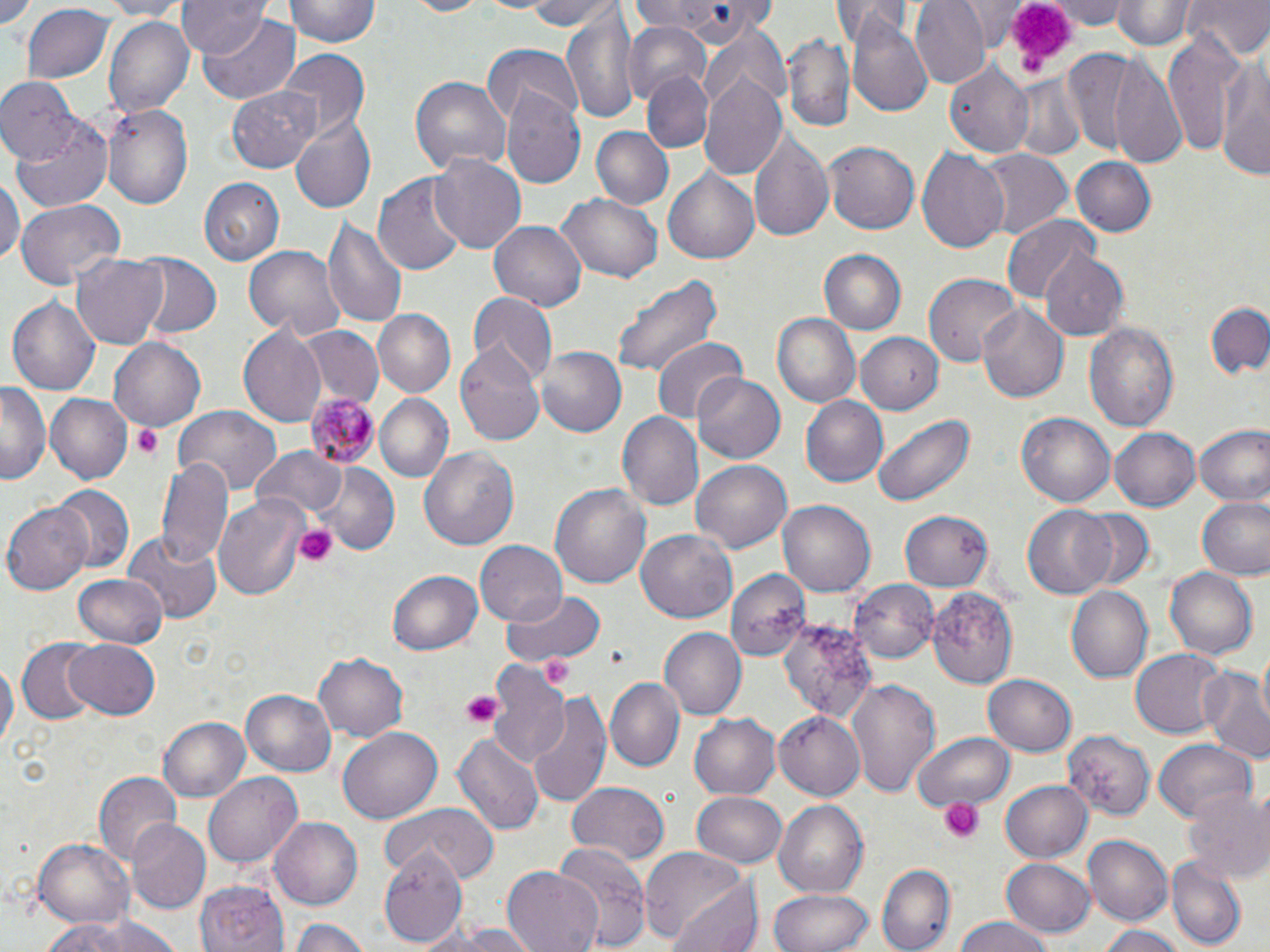

slide-level diagnosis = Plasmodium malariae
platelet locations = approximate bounding boxes as named x1/y1/x2/y2 corners in pixels: (x1=999, y1=4, x2=1075, y2=81), (x1=132, y1=425, x2=162, y2=460), (x1=294, y1=524, x2=337, y2=567), (x1=542, y1=654, x2=574, y2=688), (x1=461, y1=691, x2=500, y2=727), (x1=940, y1=797, x2=982, y2=844)
stain = May-Grünwald-Giemsa
image size = 1270×952 pixels
preparation = thin blood film
modality = light microscopy
field of view = single
Plasmodium malariae-infected red blood cell locations = approximate bounding boxes as named x1/y1/x2/y2 corners in pixels: (x1=306, y1=394, x2=379, y2=467)
magnification = 1000x
uninfected red blood cell locations = approximate bounding boxes as named x1/y1/x2/y2 corners in pixels: (x1=2, y1=0, x2=45, y2=39), (x1=91, y1=0, x2=187, y2=18), (x1=179, y1=0, x2=268, y2=58), (x1=284, y1=0, x2=382, y2=48), (x1=398, y1=0, x2=499, y2=18), (x1=518, y1=0, x2=620, y2=28), (x1=910, y1=0, x2=989, y2=87), (x1=1049, y1=0, x2=1130, y2=29), (x1=1112, y1=0, x2=1194, y2=50), (x1=1183, y1=0, x2=1269, y2=60), (x1=628, y1=1, x2=778, y2=41), (x1=833, y1=1, x2=917, y2=46), (x1=21, y1=4, x2=116, y2=86), (x1=561, y1=11, x2=642, y2=125), (x1=196, y1=13, x2=300, y2=103), (x1=103, y1=14, x2=194, y2=117), (x1=848, y1=17, x2=935, y2=116), (x1=623, y1=22, x2=714, y2=99), (x1=1164, y1=28, x2=1244, y2=162), (x1=780, y1=32, x2=854, y2=133), (x1=696, y1=44, x2=789, y2=181), (x1=482, y1=46, x2=583, y2=127), (x1=1218, y1=48, x2=1270, y2=182), (x1=278, y1=49, x2=369, y2=138), (x1=1077, y1=53, x2=1186, y2=164), (x1=946, y1=61, x2=1034, y2=157), (x1=642, y1=72, x2=713, y2=153), (x1=1007, y1=74, x2=1088, y2=162), (x1=411, y1=76, x2=511, y2=174), (x1=0, y1=79, x2=80, y2=167), (x1=227, y1=85, x2=323, y2=172), (x1=501, y1=89, x2=586, y2=189), (x1=101, y1=103, x2=193, y2=207), (x1=12, y1=114, x2=114, y2=210), (x1=292, y1=117, x2=377, y2=213), (x1=588, y1=126, x2=674, y2=211), (x1=747, y1=129, x2=833, y2=245), (x1=824, y1=140, x2=919, y2=235), (x1=916, y1=147, x2=1010, y2=256), (x1=977, y1=149, x2=1071, y2=237), (x1=431, y1=154, x2=527, y2=253), (x1=1071, y1=156, x2=1158, y2=238), (x1=662, y1=167, x2=761, y2=264), (x1=375, y1=172, x2=468, y2=275), (x1=0, y1=177, x2=22, y2=267), (x1=199, y1=178, x2=284, y2=266), (x1=556, y1=189, x2=662, y2=281), (x1=14, y1=199, x2=125, y2=290), (x1=1001, y1=217, x2=1100, y2=307), (x1=323, y1=218, x2=408, y2=327), (x1=489, y1=221, x2=588, y2=310), (x1=243, y1=246, x2=345, y2=341), (x1=818, y1=249, x2=907, y2=337), (x1=1038, y1=251, x2=1129, y2=339), (x1=70, y1=252, x2=169, y2=348), (x1=127, y1=252, x2=223, y2=341), (x1=611, y1=272, x2=721, y2=379), (x1=925, y1=272, x2=1024, y2=366), (x1=469, y1=292, x2=556, y2=384), (x1=7, y1=293, x2=100, y2=400), (x1=1209, y1=303, x2=1270, y2=379), (x1=977, y1=304, x2=1069, y2=404), (x1=374, y1=309, x2=456, y2=397), (x1=771, y1=311, x2=861, y2=411), (x1=1085, y1=320, x2=1178, y2=435), (x1=300, y1=325, x2=382, y2=405), (x1=237, y1=327, x2=326, y2=429), (x1=855, y1=331, x2=943, y2=416), (x1=109, y1=336, x2=207, y2=432), (x1=650, y1=336, x2=748, y2=425), (x1=457, y1=341, x2=545, y2=445), (x1=535, y1=346, x2=626, y2=437), (x1=691, y1=372, x2=786, y2=463), (x1=1, y1=383, x2=51, y2=486), (x1=43, y1=392, x2=132, y2=484), (x1=374, y1=394, x2=453, y2=483), (x1=802, y1=395, x2=888, y2=488), (x1=173, y1=408, x2=282, y2=499), (x1=614, y1=410, x2=702, y2=510), (x1=871, y1=412, x2=975, y2=510), (x1=1017, y1=414, x2=1114, y2=507), (x1=1193, y1=424, x2=1270, y2=507), (x1=1109, y1=427, x2=1199, y2=512), (x1=419, y1=447, x2=519, y2=553), (x1=252, y1=448, x2=348, y2=521), (x1=155, y1=455, x2=232, y2=570), (x1=691, y1=460, x2=791, y2=552), (x1=318, y1=465, x2=400, y2=553), (x1=550, y1=482, x2=651, y2=592), (x1=49, y1=484, x2=133, y2=577), (x1=214, y1=494, x2=310, y2=598), (x1=1196, y1=495, x2=1270, y2=580), (x1=778, y1=500, x2=875, y2=598), (x1=4, y1=501, x2=93, y2=595), (x1=1022, y1=505, x2=1119, y2=599), (x1=1072, y1=508, x2=1159, y2=593), (x1=899, y1=511, x2=993, y2=593), (x1=636, y1=531, x2=737, y2=623), (x1=122, y1=532, x2=220, y2=624), (x1=474, y1=541, x2=566, y2=627), (x1=1165, y1=567, x2=1259, y2=663), (x1=725, y1=569, x2=810, y2=660), (x1=388, y1=570, x2=483, y2=658), (x1=73, y1=574, x2=167, y2=649), (x1=850, y1=579, x2=939, y2=664), (x1=1066, y1=586, x2=1153, y2=683), (x1=501, y1=587, x2=603, y2=672), (x1=929, y1=587, x2=1019, y2=689), (x1=780, y1=618, x2=878, y2=726), (x1=660, y1=627, x2=748, y2=720), (x1=16, y1=639, x2=100, y2=723), (x1=61, y1=639, x2=161, y2=720), (x1=1130, y1=647, x2=1227, y2=739), (x1=312, y1=652, x2=408, y2=741), (x1=0, y1=655, x2=15, y2=760), (x1=489, y1=662, x2=574, y2=778), (x1=1201, y1=668, x2=1270, y2=763), (x1=983, y1=675, x2=1075, y2=756), (x1=848, y1=676, x2=943, y2=800), (x1=604, y1=677, x2=685, y2=772), (x1=242, y1=689, x2=335, y2=778), (x1=527, y1=691, x2=611, y2=810), (x1=774, y1=710, x2=866, y2=799), (x1=689, y1=713, x2=781, y2=799), (x1=157, y1=715, x2=250, y2=800), (x1=337, y1=728, x2=440, y2=824), (x1=1062, y1=729, x2=1155, y2=819), (x1=452, y1=731, x2=545, y2=836), (x1=915, y1=731, x2=1014, y2=812), (x1=1153, y1=740, x2=1256, y2=821), (x1=203, y1=772, x2=302, y2=867), (x1=93, y1=773, x2=180, y2=868), (x1=999, y1=778, x2=1093, y2=863), (x1=567, y1=781, x2=669, y2=866), (x1=1186, y1=787, x2=1270, y2=885), (x1=691, y1=792, x2=787, y2=870), (x1=772, y1=800, x2=868, y2=898), (x1=378, y1=803, x2=499, y2=885), (x1=270, y1=816, x2=366, y2=910), (x1=124, y1=819, x2=211, y2=916), (x1=1085, y1=834, x2=1174, y2=927), (x1=33, y1=838, x2=132, y2=928), (x1=549, y1=844, x2=654, y2=952), (x1=380, y1=848, x2=465, y2=946), (x1=639, y1=848, x2=757, y2=949), (x1=1000, y1=857, x2=1097, y2=939), (x1=1165, y1=858, x2=1247, y2=946), (x1=504, y1=865, x2=604, y2=952), (x1=878, y1=865, x2=956, y2=952), (x1=198, y1=879, x2=287, y2=952), (x1=767, y1=888, x2=873, y2=952), (x1=42, y1=914, x2=183, y2=952), (x1=289, y1=917, x2=375, y2=951), (x1=951, y1=918, x2=1059, y2=952), (x1=416, y1=923, x2=541, y2=952), (x1=1096, y1=924, x2=1187, y2=952)